Classify this cell by malaria status.
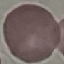

It is uninfected.

preparation = thin blood smear
capture = smartphone camera at the microscope eyepiece
image type = automatically extracted cell patch, resized to 64 × 64 pixels
stain = Giemsa